Outline each Plasmodium malariae-infected red blood cell.
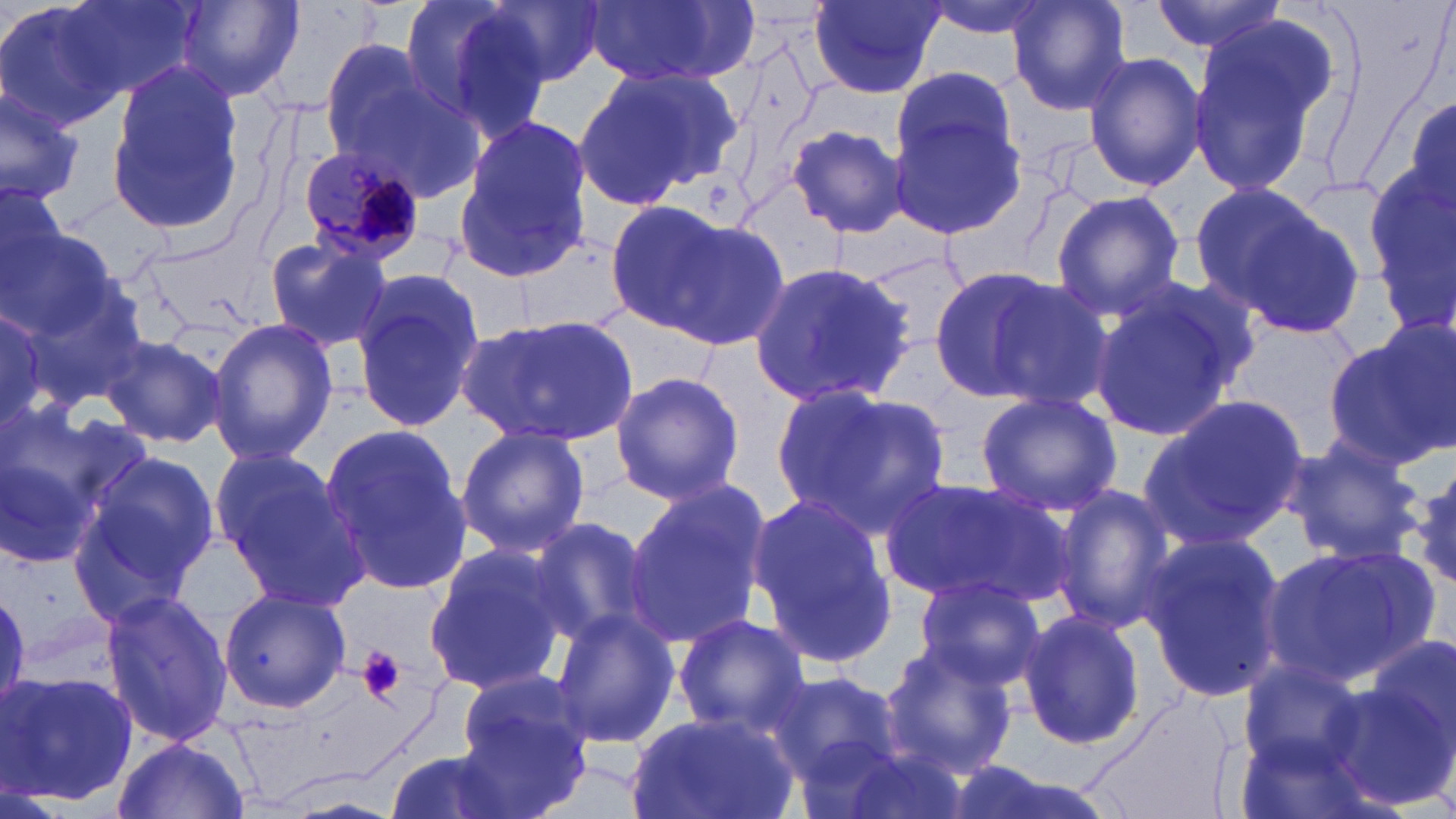

Approximate bounding boxes as (x1,y1)-(x2,y2) corner pairs in pixels.
Plasmodium malariae-infected red blood cells: (294,144)-(424,263).

Uninfected red blood cell locations: (0,0)-(126,133), (58,0)-(200,103), (402,0)-(554,139), (487,0)-(606,84), (586,0)-(758,87), (921,0)-(1059,40), (1006,0)-(1134,116), (1149,0)-(1290,55), (172,1)-(304,103), (807,1)-(942,99), (1187,14)-(1335,201), (315,34)-(451,169), (1082,52)-(1206,192), (103,59)-(250,240), (570,63)-(737,214), (891,67)-(1017,178), (0,81)-(85,206), (1406,96)-(1456,210), (888,111)-(1026,238), (451,118)-(591,285), (785,123)-(907,239), (1368,164)-(1456,324), (1,176)-(74,315), (1192,184)-(1363,337), (1049,189)-(1185,319), (600,198)-(746,337), (0,211)-(120,345), (660,217)-(792,354), (261,236)-(395,354), (749,260)-(917,406), (926,263)-(1076,406), (352,270)-(483,432), (979,275)-(1118,414), (1086,282)-(1250,445), (20,285)-(151,408), (0,312)-(56,435), (463,312)-(639,448), (208,318)-(336,464), (1328,324)-(1456,471), (101,333)-(232,450), (609,370)-(745,504), (774,385)-(949,532), (975,390)-(1122,518), (1140,396)-(1307,550), (0,417)-(117,571), (320,424)-(472,593), (455,424)-(591,557), (1278,438)-(1426,568), (73,449)-(225,618), (215,452)-(372,613), (1403,464)-(1456,597), (881,476)-(1067,609), (622,479)-(771,651), (1053,482)-(1177,633), (747,494)-(897,666), (528,516)-(657,649), (1137,530)-(1288,703), (422,543)-(570,697), (1257,544)-(1426,687), (913,577)-(1044,688), (217,586)-(350,715), (98,588)-(232,748), (547,608)-(680,750), (1018,610)-(1149,752), (672,615)-(809,737), (1368,632)-(1456,756), (876,647)-(1019,778), (1239,659)-(1365,770), (2,669)-(137,807), (764,669)-(903,783), (458,670)-(594,815), (1332,671)-(1454,813), (1081,692)-(1241,819), (625,708)-(798,819), (1232,731)-(1376,819), (112,736)-(252,819), (807,743)-(969,819), (386,749)-(519,819), (276,793)-(406,818). Platelet locations: (358,646)-(407,702). Slide-level diagnosis: Plasmodium malariae. Optical microscopy. Thin blood film. Image is 1456×819 pixels. Single field of view. Captured at 1000x magnification. May-Grünwald-Giemsa-stained preparation.